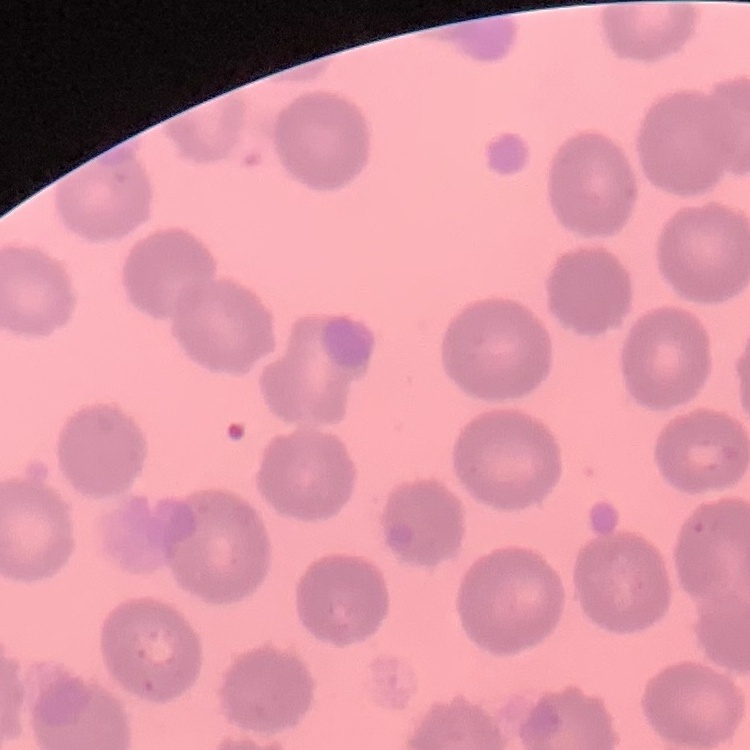
erythrocyte morphology = no rouleaux formation
preparation = thin blood smear
image type = one tile cut from a larger photomicrograph
stain = Field's or Giemsa